Locate every Plasmodium falciparum-infected red blood cell.
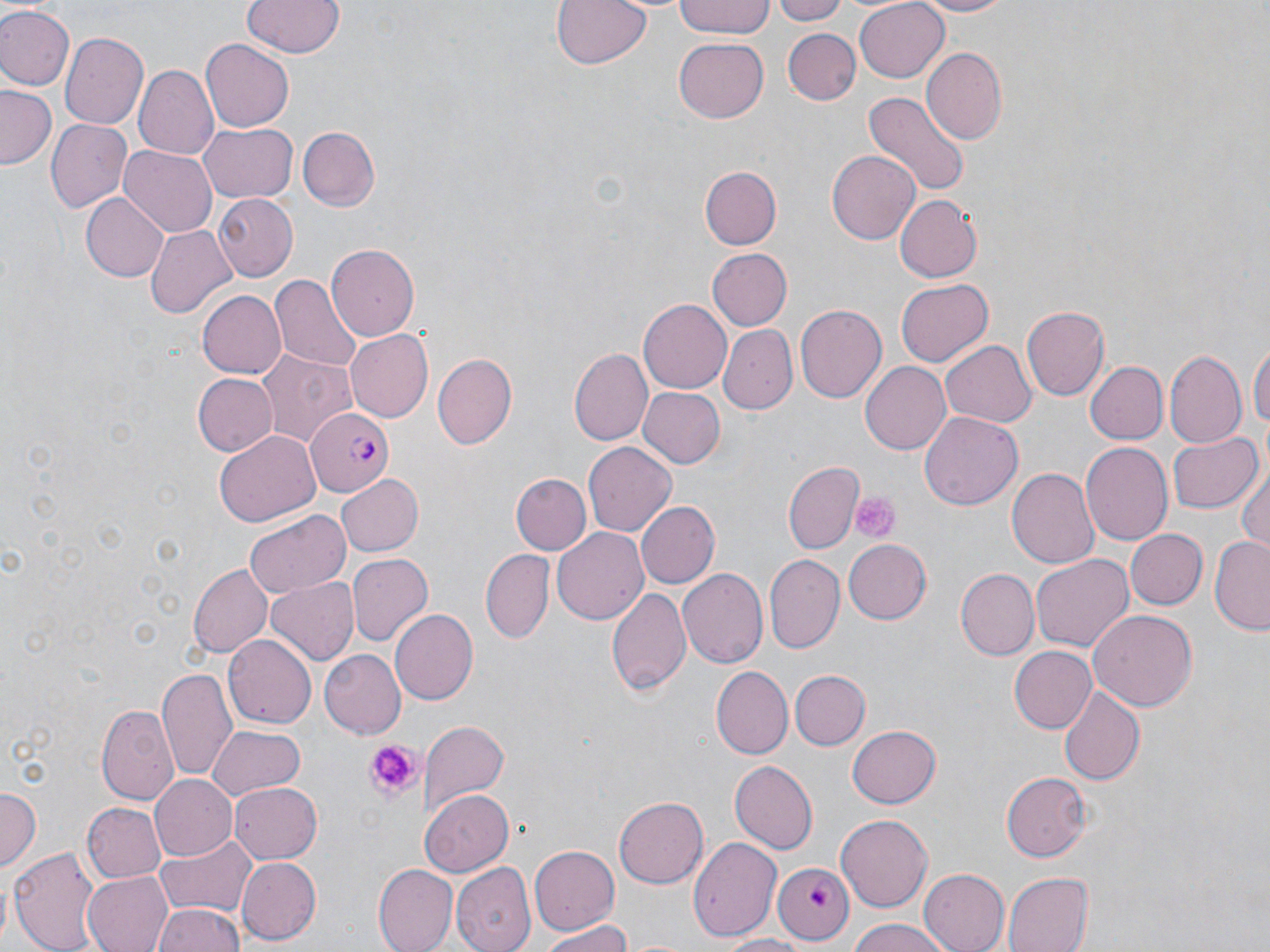
Approximate bounding boxes as (x1,y1)-(x2,y2) corner pairs in pixels.
Plasmodium falciparum-infected red blood cells: (305,407)-(394,494), (775,863)-(857,945).

slide-level diagnosis = Plasmodium falciparum
uninfected red blood cell locations = approximate bounding boxes as (x1,y1)-(x2,y2) corner pairs in pixels: (241,0)-(344,58), (548,0)-(653,72), (672,0)-(775,39), (772,0)-(847,23), (903,0)-(1019,17), (853,1)-(950,82), (0,5)-(74,89), (782,28)-(860,105), (58,31)-(147,129), (674,35)-(769,121), (201,38)-(294,133), (920,47)-(1006,143), (134,66)-(217,158), (1,85)-(58,171), (862,90)-(971,201), (44,119)-(132,214), (198,123)-(297,203), (298,126)-(380,211), (119,145)-(216,236), (827,149)-(922,245), (699,167)-(779,249), (81,194)-(168,280), (213,194)-(297,279), (890,194)-(986,282), (145,227)-(235,318), (327,244)-(420,340), (709,249)-(793,331), (271,273)-(362,370), (897,280)-(993,367), (197,291)-(286,378), (638,298)-(733,394), (795,306)-(885,402), (1022,306)-(1110,400), (720,323)-(796,414), (343,328)-(433,423), (941,339)-(1036,427), (1250,342)-(1270,441), (253,347)-(357,448), (569,347)-(653,445), (1165,349)-(1247,449), (433,353)-(518,449), (1085,360)-(1166,445), (861,361)-(953,455), (193,372)-(279,456), (639,388)-(724,467), (921,413)-(1022,509), (1165,430)-(1260,514), (214,432)-(321,528), (1081,442)-(1173,545), (583,443)-(676,537), (783,461)-(863,552), (1234,463)-(1270,556), (1008,467)-(1101,571), (333,473)-(423,556), (511,473)-(589,554), (635,500)-(718,589), (245,511)-(349,598), (1124,526)-(1207,608), (551,527)-(649,624), (1209,535)-(1270,634), (841,538)-(932,625), (480,550)-(554,644), (1031,553)-(1133,652), (346,554)-(431,646), (765,554)-(845,653), (187,563)-(272,658), (678,567)-(768,669), (955,568)-(1038,659), (265,577)-(359,663), (608,586)-(693,700), (1086,609)-(1199,711), (390,610)-(478,707), (224,637)-(314,729), (1008,645)-(1097,734), (317,650)-(405,739), (711,667)-(792,759), (157,668)-(239,783), (789,670)-(871,750), (1057,688)-(1146,787), (96,706)-(178,806), (423,720)-(509,811), (846,724)-(942,808), (207,729)-(305,802), (728,761)-(817,854), (1000,769)-(1090,863), (149,773)-(238,861), (229,781)-(322,865), (0,788)-(41,871), (421,790)-(512,876), (612,796)-(707,888), (82,802)-(166,882), (835,814)-(931,910), (156,833)-(258,919), (689,837)-(780,941), (10,845)-(102,952), (530,846)-(619,934), (235,856)-(321,944), (453,864)-(536,951), (374,865)-(456,951), (918,868)-(1010,952), (82,871)-(176,952), (1002,872)-(1093,952), (153,903)-(246,952), (842,919)-(956,951), (534,923)-(636,951), (712,934)-(809,951)
image size = 1270×952 pixels
preparation = thin blood film
field of view = single
platelet locations = approximate bounding boxes as (x1,y1)-(x2,y2) corner pairs in pixels: (852,492)-(899,540), (360,738)-(419,800)
magnification = 1000x
modality = light microscopy
stain = May-Grünwald-Giemsa